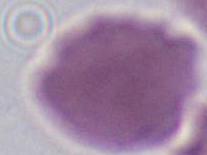

1000x magnification. An erythrocyte is seen. Micrograph.